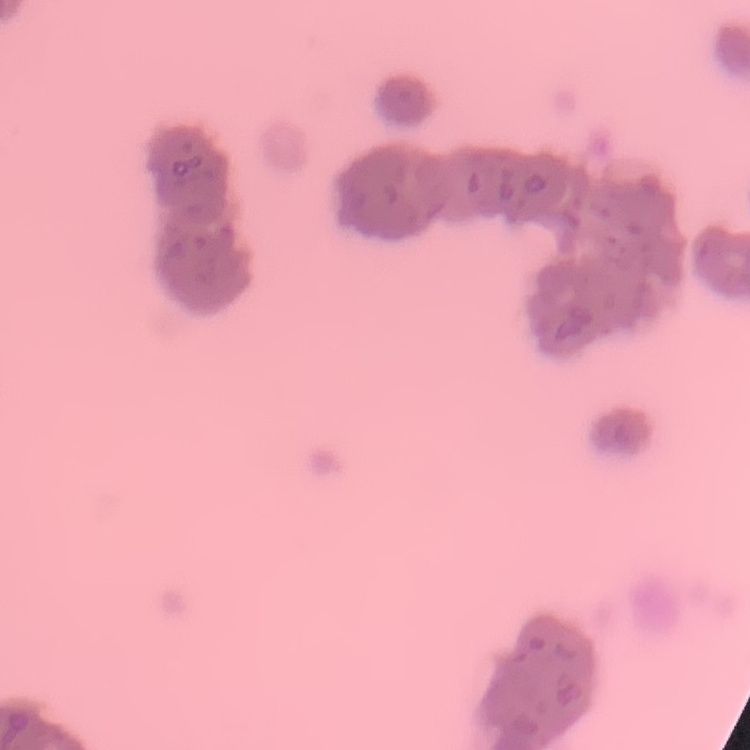 The erythrocytes show rouleaux formation. Field's or Giemsa stain. Square crop of a larger photomicrograph. Thin blood smear.